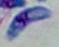

Summary:
  - Modality: micrograph
  - Identification: Toxoplasma gondii
  - Magnification: 1000x